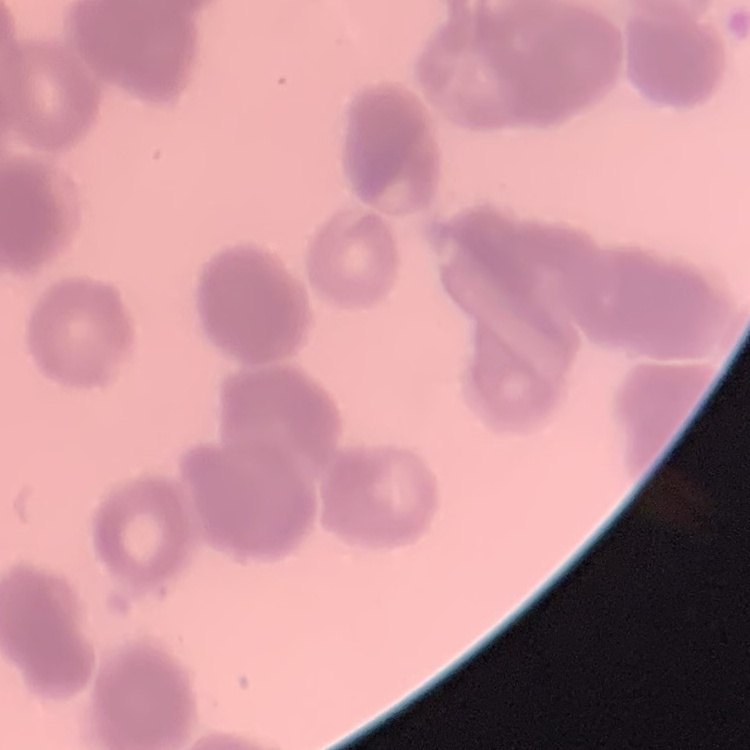
The red blood cells exhibit rouleaux formation. One tile cut from a larger photomicrograph. Thin peripheral smear. Stained with either Field's or Giemsa.